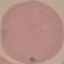
Result: no malaria parasites seen. Giemsa-stained preparation. Automatically extracted cell patch, resized to 64 × 64 pixels. Acquired by smartphone through the microscope eyepiece. Thin blood film.